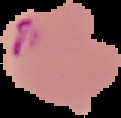

preparation = thin blood film
result = Plasmodium parasites identified
image size = 121×118 pixels
image type = cell region segmented out of the field of view; surrounding area masked to black